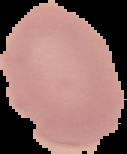
Segmented cell region on a black background. Malaria status: uninfected. Image is 127×154 pixels. From a thin blood smear.